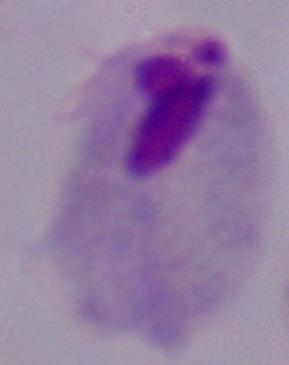
A trichomonad is shown. Micrograph. Captured at 1000x magnification.